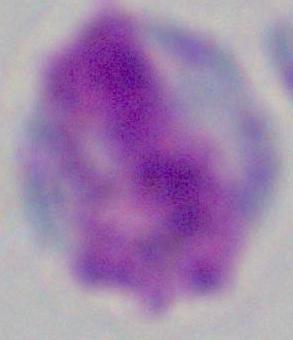 A leukocyte is seen. Captured at 1000x magnification. Photomicrograph.